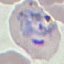

Summary:
  - Result: malaria parasites detected
  - Preparation: thin blood smear
  - Stain: Giemsa
  - Capture: smartphone camera at the microscope eyepiece
  - Image type: cell patch, automatically extracted from a larger field of view and resized to 64 × 64 pixels